Report the malaria status of this cell.
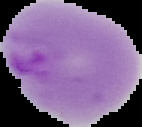
It is parasitized.

Image is 142×127 pixels. From a thin blood film. Cell region segmented out of the field of view; the surrounding area is masked to black.